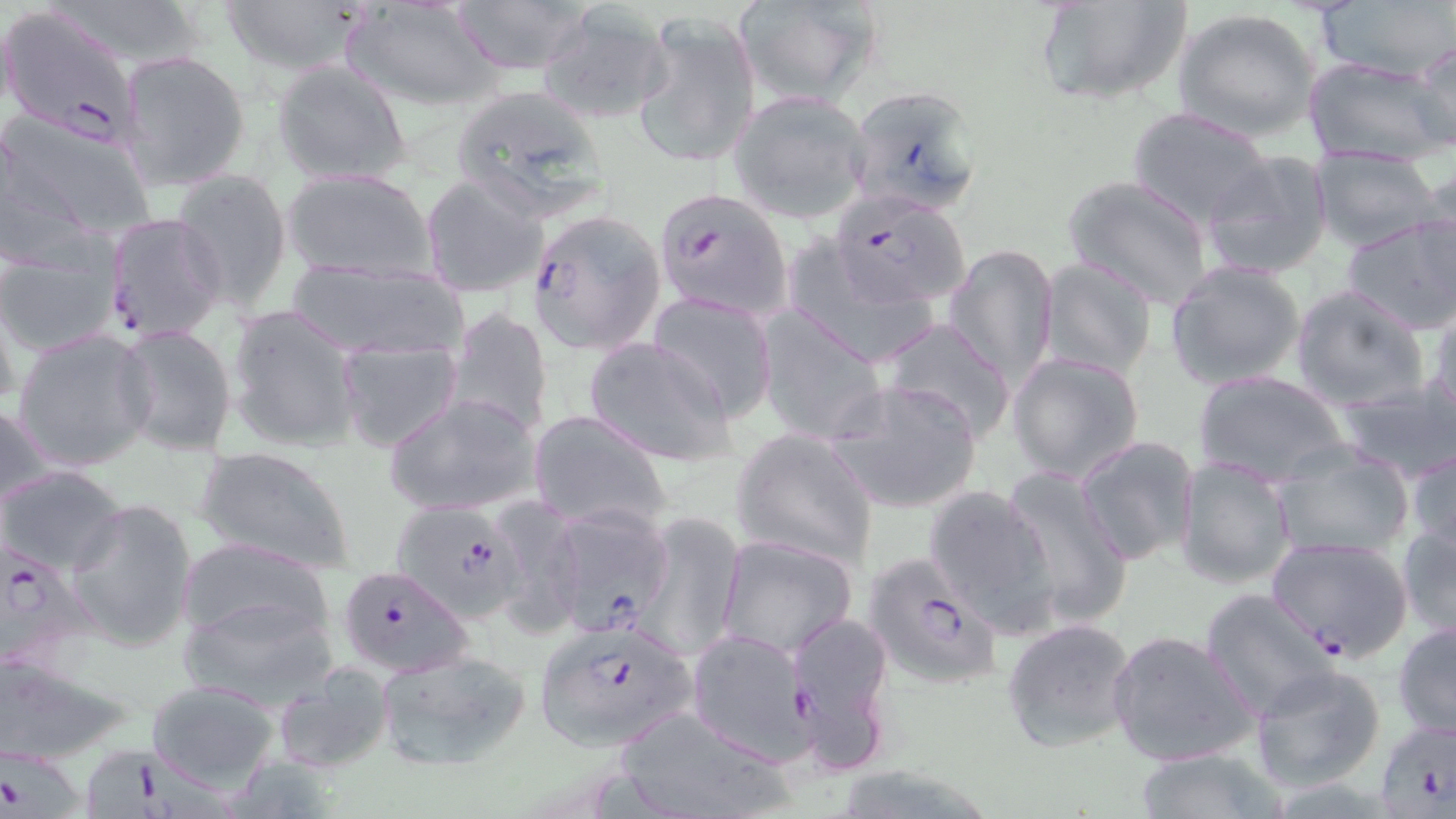
Approximate bounding boxes as named x1/y1/x2/y2 corners in pixels. Plasmodium falciparum-infected red blood cell locations: (x1=0, y1=6, x2=140, y2=145), (x1=847, y1=85, x2=983, y2=219), (x1=651, y1=186, x2=792, y2=322), (x1=831, y1=192, x2=971, y2=308), (x1=528, y1=206, x2=663, y2=356), (x1=103, y1=212, x2=226, y2=342), (x1=544, y1=502, x2=679, y2=638), (x1=395, y1=503, x2=520, y2=626), (x1=1265, y1=534, x2=1414, y2=663), (x1=1, y1=539, x2=98, y2=676), (x1=859, y1=553, x2=1006, y2=693), (x1=337, y1=563, x2=473, y2=677), (x1=531, y1=616, x2=700, y2=748), (x1=686, y1=629, x2=813, y2=762), (x1=1374, y1=719, x2=1454, y2=814), (x1=1, y1=737, x2=92, y2=819), (x1=87, y1=745, x2=235, y2=818). Uninfected red blood cell locations: (x1=214, y1=0, x2=373, y2=75), (x1=342, y1=0, x2=504, y2=110), (x1=448, y1=0, x2=602, y2=75), (x1=735, y1=0, x2=886, y2=107), (x1=1031, y1=0, x2=1194, y2=106), (x1=1316, y1=0, x2=1453, y2=83), (x1=536, y1=7, x2=672, y2=125), (x1=1174, y1=7, x2=1323, y2=140), (x1=632, y1=11, x2=761, y2=169), (x1=1411, y1=39, x2=1456, y2=151), (x1=120, y1=49, x2=251, y2=190), (x1=1302, y1=55, x2=1449, y2=166), (x1=270, y1=58, x2=412, y2=186), (x1=448, y1=87, x2=609, y2=222), (x1=728, y1=90, x2=875, y2=222), (x1=1126, y1=106, x2=1273, y2=228), (x1=1, y1=109, x2=158, y2=248), (x1=1310, y1=145, x2=1443, y2=252), (x1=1200, y1=150, x2=1335, y2=281), (x1=172, y1=168, x2=292, y2=312), (x1=282, y1=168, x2=437, y2=282), (x1=1063, y1=174, x2=1215, y2=308), (x1=420, y1=175, x2=547, y2=298), (x1=1341, y1=213, x2=1456, y2=337), (x1=783, y1=241, x2=942, y2=372), (x1=944, y1=243, x2=1058, y2=388), (x1=1, y1=245, x2=122, y2=359), (x1=1037, y1=256, x2=1159, y2=379), (x1=281, y1=259, x2=471, y2=362), (x1=1165, y1=261, x2=1309, y2=392), (x1=1289, y1=284, x2=1430, y2=410), (x1=648, y1=293, x2=779, y2=422), (x1=1427, y1=300, x2=1456, y2=432), (x1=225, y1=303, x2=364, y2=453), (x1=754, y1=306, x2=886, y2=445), (x1=446, y1=307, x2=553, y2=438), (x1=878, y1=317, x2=1017, y2=443), (x1=113, y1=322, x2=241, y2=457), (x1=12, y1=327, x2=156, y2=473), (x1=336, y1=335, x2=464, y2=452), (x1=582, y1=336, x2=734, y2=463), (x1=1009, y1=352, x2=1147, y2=484), (x1=1194, y1=371, x2=1349, y2=484), (x1=825, y1=378, x2=982, y2=515), (x1=1333, y1=378, x2=1456, y2=480), (x1=383, y1=392, x2=543, y2=517), (x1=1, y1=400, x2=52, y2=513), (x1=530, y1=409, x2=672, y2=534), (x1=731, y1=428, x2=879, y2=568), (x1=1075, y1=434, x2=1200, y2=565), (x1=1406, y1=443, x2=1456, y2=561), (x1=1269, y1=445, x2=1414, y2=563), (x1=192, y1=446, x2=355, y2=572), (x1=1173, y1=456, x2=1296, y2=591), (x1=0, y1=465, x2=128, y2=577), (x1=1001, y1=466, x2=1133, y2=628), (x1=921, y1=482, x2=1061, y2=632), (x1=67, y1=499, x2=197, y2=652), (x1=485, y1=499, x2=586, y2=636), (x1=638, y1=509, x2=748, y2=659), (x1=1396, y1=520, x2=1456, y2=640), (x1=715, y1=535, x2=859, y2=660), (x1=178, y1=538, x2=336, y2=660), (x1=1199, y1=588, x2=1340, y2=721), (x1=178, y1=589, x2=342, y2=709), (x1=786, y1=609, x2=897, y2=772), (x1=1001, y1=617, x2=1138, y2=751), (x1=1392, y1=620, x2=1455, y2=742), (x1=1107, y1=629, x2=1258, y2=767), (x1=374, y1=646, x2=532, y2=771), (x1=0, y1=654, x2=137, y2=764), (x1=1251, y1=661, x2=1388, y2=792), (x1=272, y1=662, x2=396, y2=774), (x1=143, y1=677, x2=282, y2=789), (x1=607, y1=704, x2=796, y2=819), (x1=1130, y1=746, x2=1287, y2=817). Slide-level diagnosis: Plasmodium falciparum. Thin blood smear. One field of a larger specimen. 1000x magnification. Optical microscopy. May-Grünwald-Giemsa-stained preparation. Image is 1456×819 pixels.